Classify this cell by malaria status.
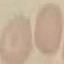

Uninfected.

Thin blood smear. Photographed with a smartphone camera at the microscope eyepiece. Cell patch, automatically extracted from a larger field of view and resized to 64 × 64 pixels. Giemsa stain.